Identify the parasite.
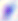
This is Toxoplasma gondii.

{
  "magnification": "400x",
  "modality": "micrograph"
}